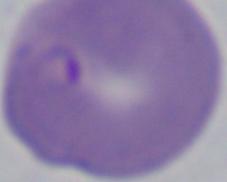
Summary:
  - Magnification: 1000x
  - Identification: Babesia
  - Modality: photomicrograph